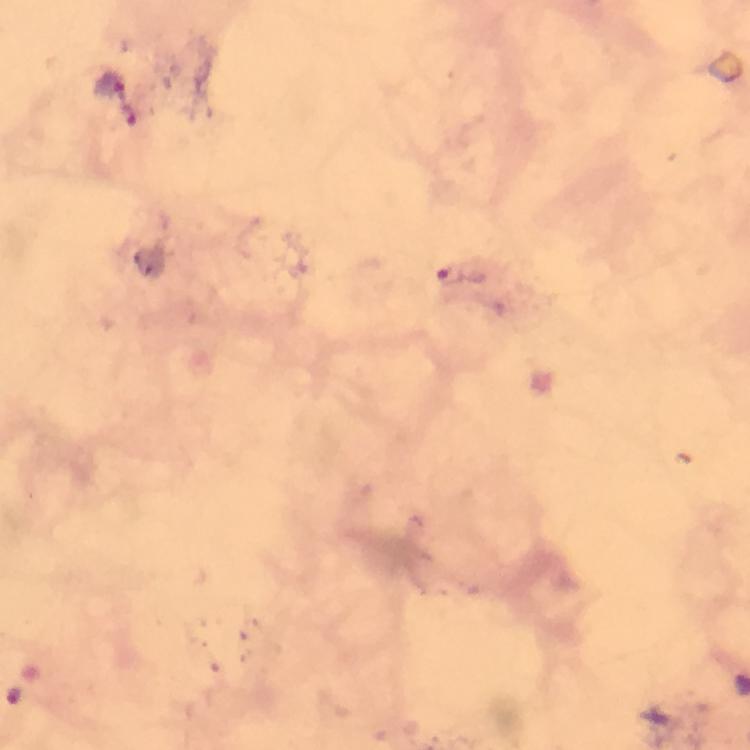

Approximate centers as (x, y) in pixels. Malaria parasite locations: (108, 86), (137, 122), (451, 275). From a malaria diagnostic workup. Giemsa stain. Thick blood smear. 100x magnification. Immersion oil applied. Cropped region of a single field of view. Photographed through the microscope with a smartphone camera. Image is 750×750 pixels.